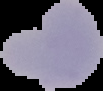

Summary:
  - Preparation: thin blood smear
  - Result: malaria parasites identified
  - Image size: 103×91 pixels
  - Image type: cell region segmented out of the field of view; surrounding area masked to black